Identify the parasite.
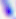

Toxoplasma gondii.

400x magnification. Photomicrograph.